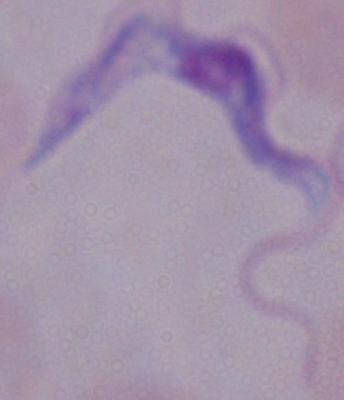

Summary:
  - Identification: trypanosome
  - Magnification: 1000x
  - Modality: micrograph